Report the malaria status of this cell.
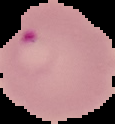

It is parasitized.

Summary:
  - Image type: cell region segmented out of the field of view; surrounding area masked to black
  - Image size: 115×124 pixels
  - Preparation: thin blood smear